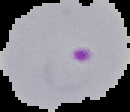
Summary:
  - Preparation: thin blood film
  - Image type: cell region segmented out of the field of view; surrounding area masked to black
  - Image size: 130×112 pixels
  - Malaria status: parasitized